Assess this cell for malaria.
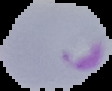

Parasitized.

image_size: 112×91 pixels
preparation: thin blood smear
image_type: segmented cell region on a black background